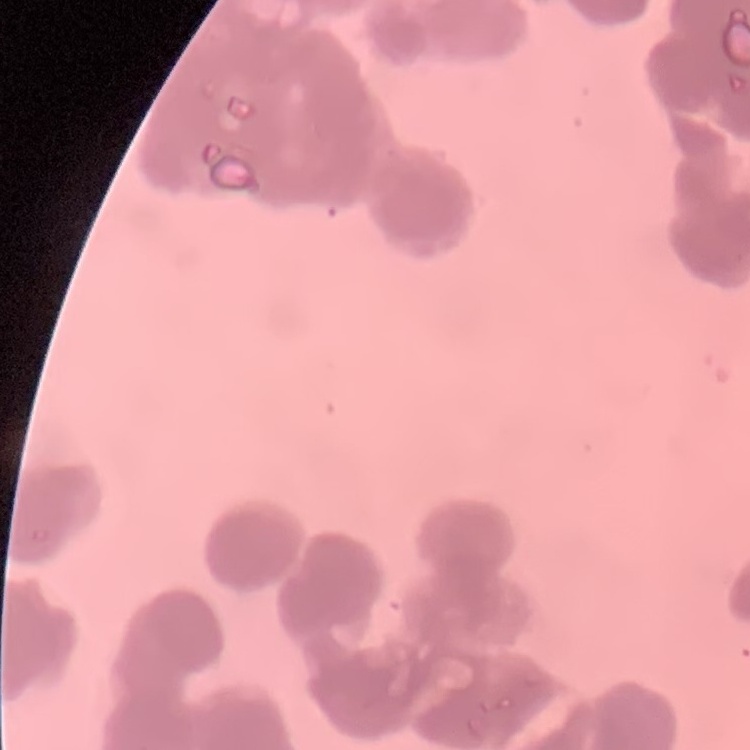

erythrocyte morphology = rouleaux formation
image type = square crop of a larger photomicrograph
stain = Field's or Giemsa
preparation = thin blood smear